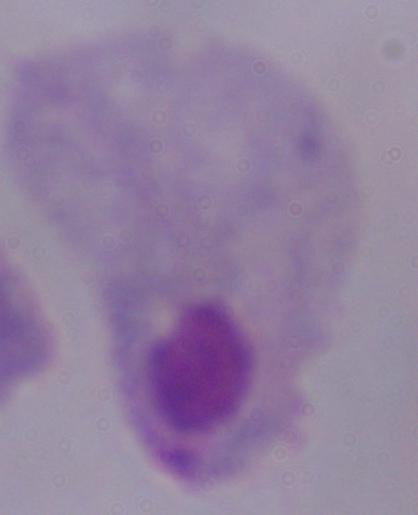
Captured at 1000x magnification. Micrograph. A trichomonad is seen.